State which cell type is depicted.
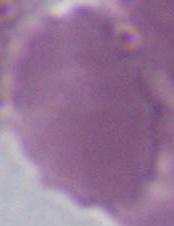
An erythrocyte.

Captured at 1000x magnification. Micrograph.